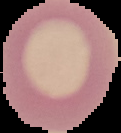

Cell region segmented out of the field of view; the surrounding area is masked to black. Image is 121×133 pixels. Malaria status: uninfected. From a thin blood film.